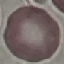
Summary:
  - Malaria status: uninfected
  - Stain: Giemsa
  - Preparation: thin blood film
  - Capture: smartphone camera at the microscope eyepiece
  - Image type: automatically extracted cell patch, resized to 64 × 64 pixels